Describe the morphology of the erythrocytes.
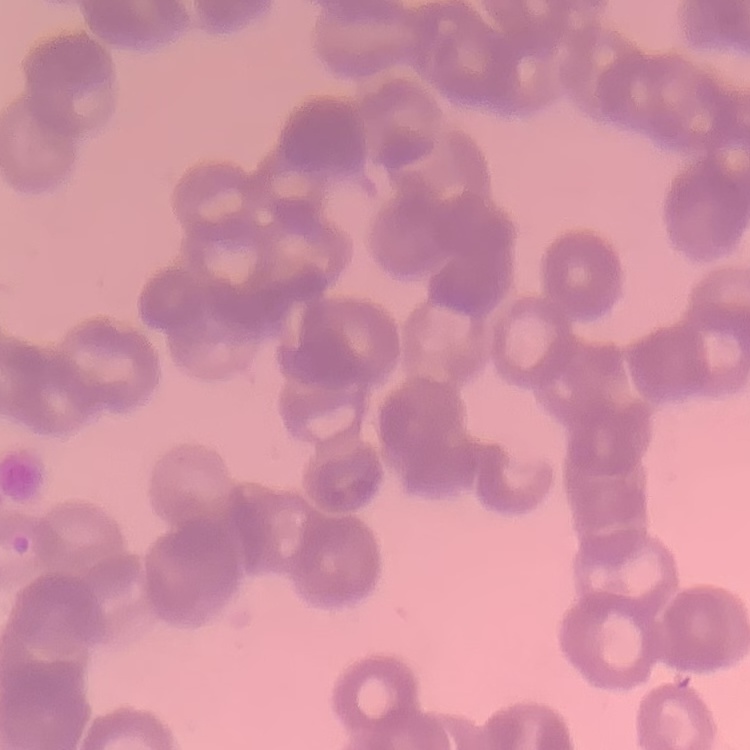
Rouleaux formation.

Thin peripheral smear. One tile cut from a larger photomicrograph. Stained with either Field's or Giemsa.